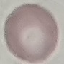 Result: no malaria parasites seen. Acquired by smartphone through the microscope eyepiece. Automatically extracted cell patch, resized to 64 × 64 pixels. Giemsa stain. Thin smear of blood.